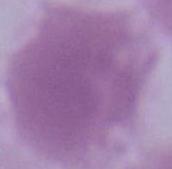
Micrograph. 1000x magnification. An erythrocyte is seen.